Name the parasite shown.
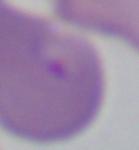

This is Babesia.

magnification = 1000x
modality = micrograph